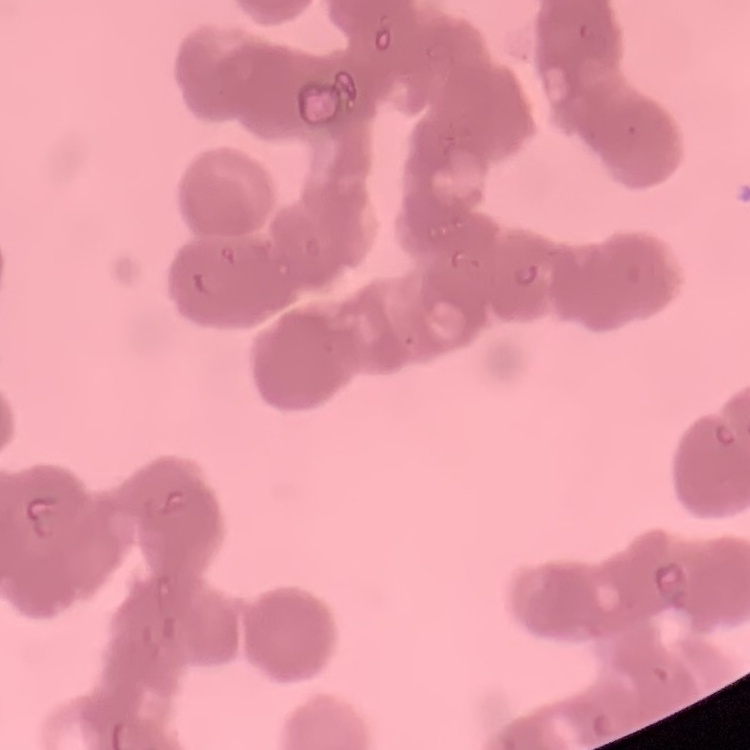
Summary:
  - Red blood cell morphology: rouleaux formation
  - Stain: Field's or Giemsa
  - Preparation: thin peripheral smear
  - Image type: square crop of a larger photomicrograph